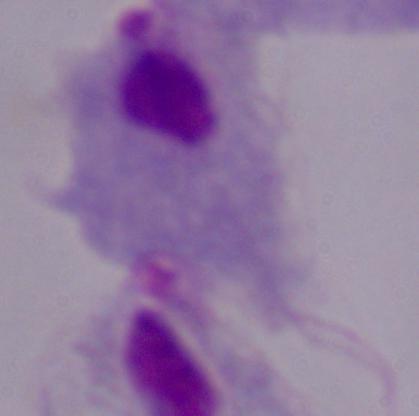
Summary:
  - Modality: micrograph
  - Magnification: 1000x
  - Identification: trichomonad